Assess this cell for malaria.
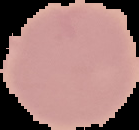

Uninfected.

Summary:
  - Image type: segmented cell region on a black background
  - Preparation: thin blood smear
  - Image size: 139×130 pixels